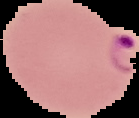

result = malaria parasites detected
preparation = thin blood smear
image size = 139×118 pixels
image type = segmented cell region with the area outside set to black